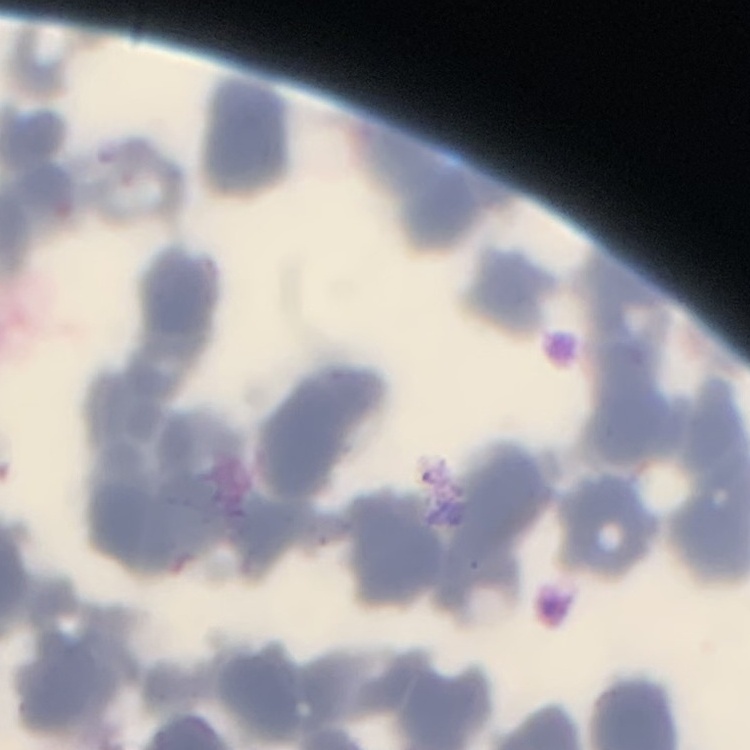

The erythrocytes show rouleaux formation. Square crop of a larger photomicrograph. Field's or Giemsa stain. Thin peripheral smear.